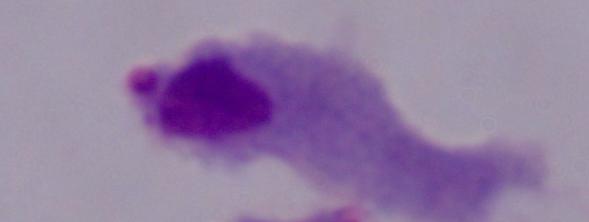 Captured at 1000x magnification. Micrograph. A trichomonad is seen.